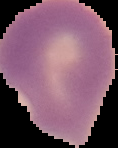
Image is 118×148 pixels. Segmented cell region on a black background. From a thin blood smear. Result: Plasmodium parasites identified.